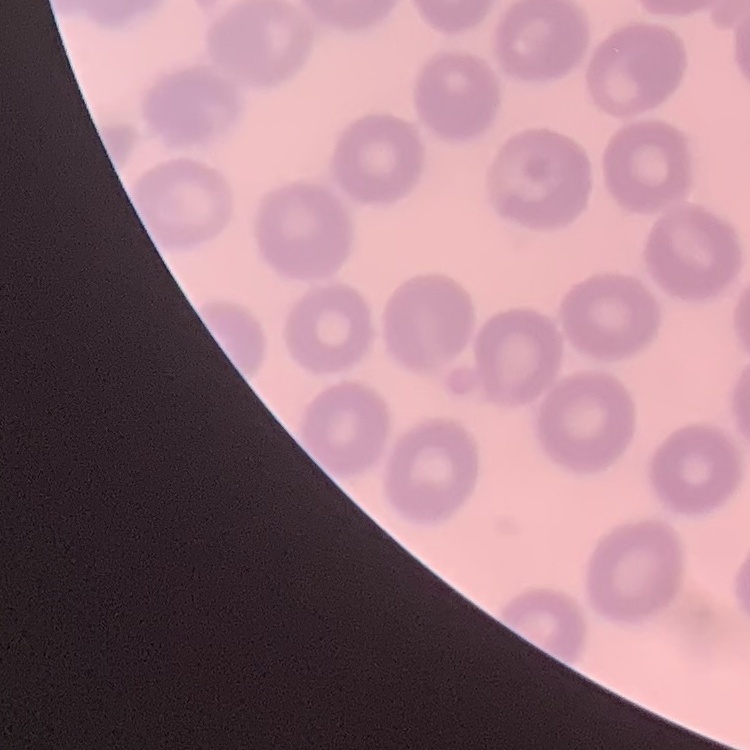

Summary:
  - Erythrocyte morphology: no rouleaux formation
  - Image type: one tile cut from a larger photomicrograph
  - Stain: Field's or Giemsa
  - Preparation: thin blood smear